Identify the parasite.
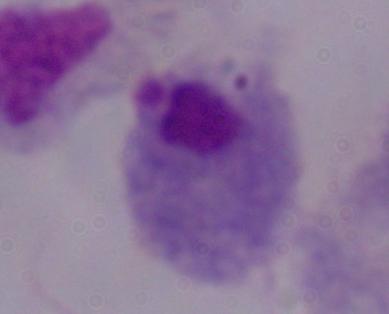

This is a trichomonad.

Micrograph. 1000x magnification.